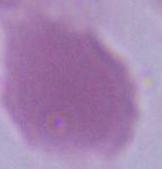 1000x magnification. A red blood cell is shown. Micrograph.